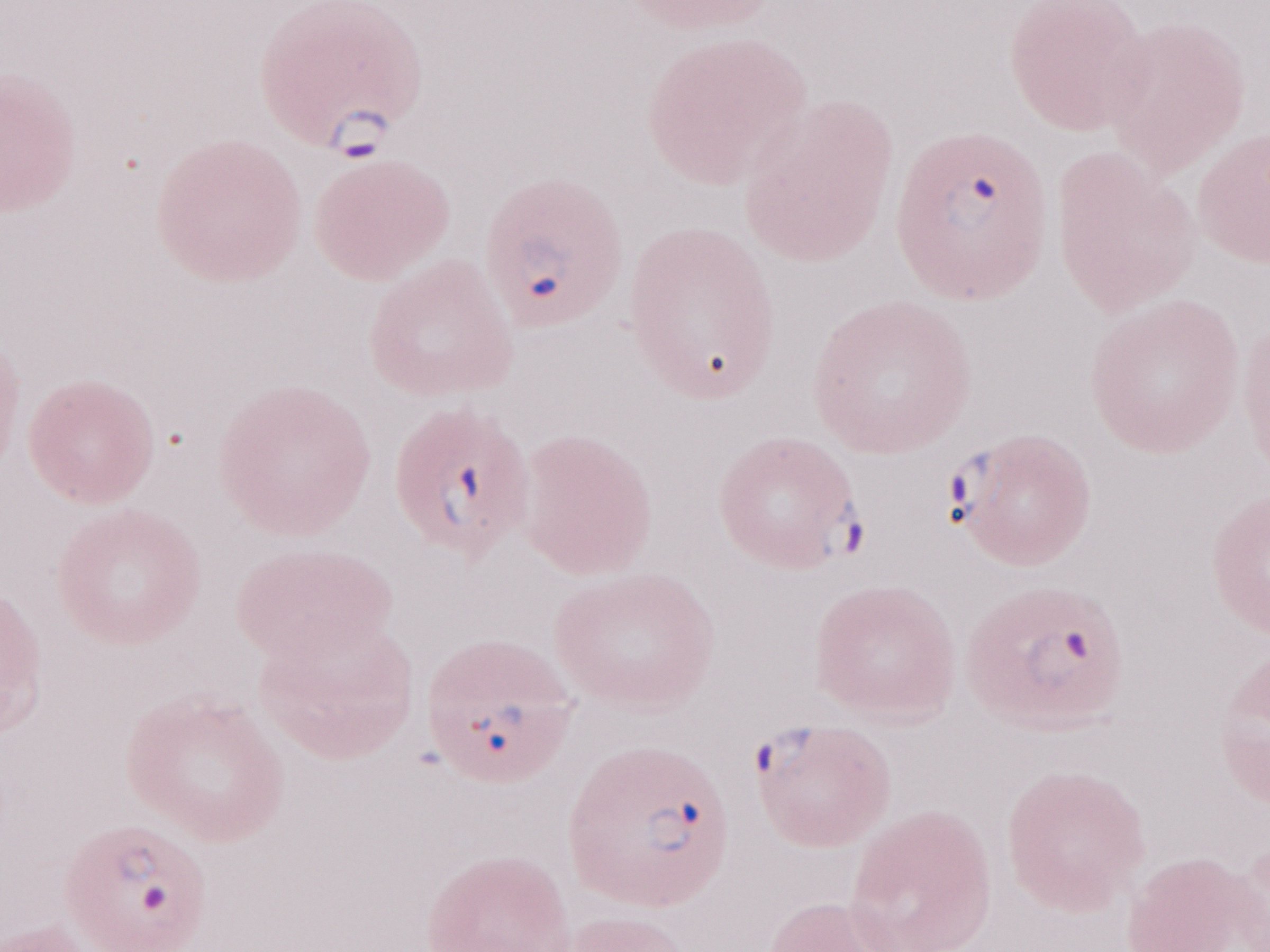 Magnification: 1,000x. Olympus BX43 microscope, Olympus DP73 camera. Image is 1270×952 pixels. Thin blood film. Single field of view. May-Grünwald-Giemsa (MGG) stain. Malaria diagnosis (patient-level): positive.